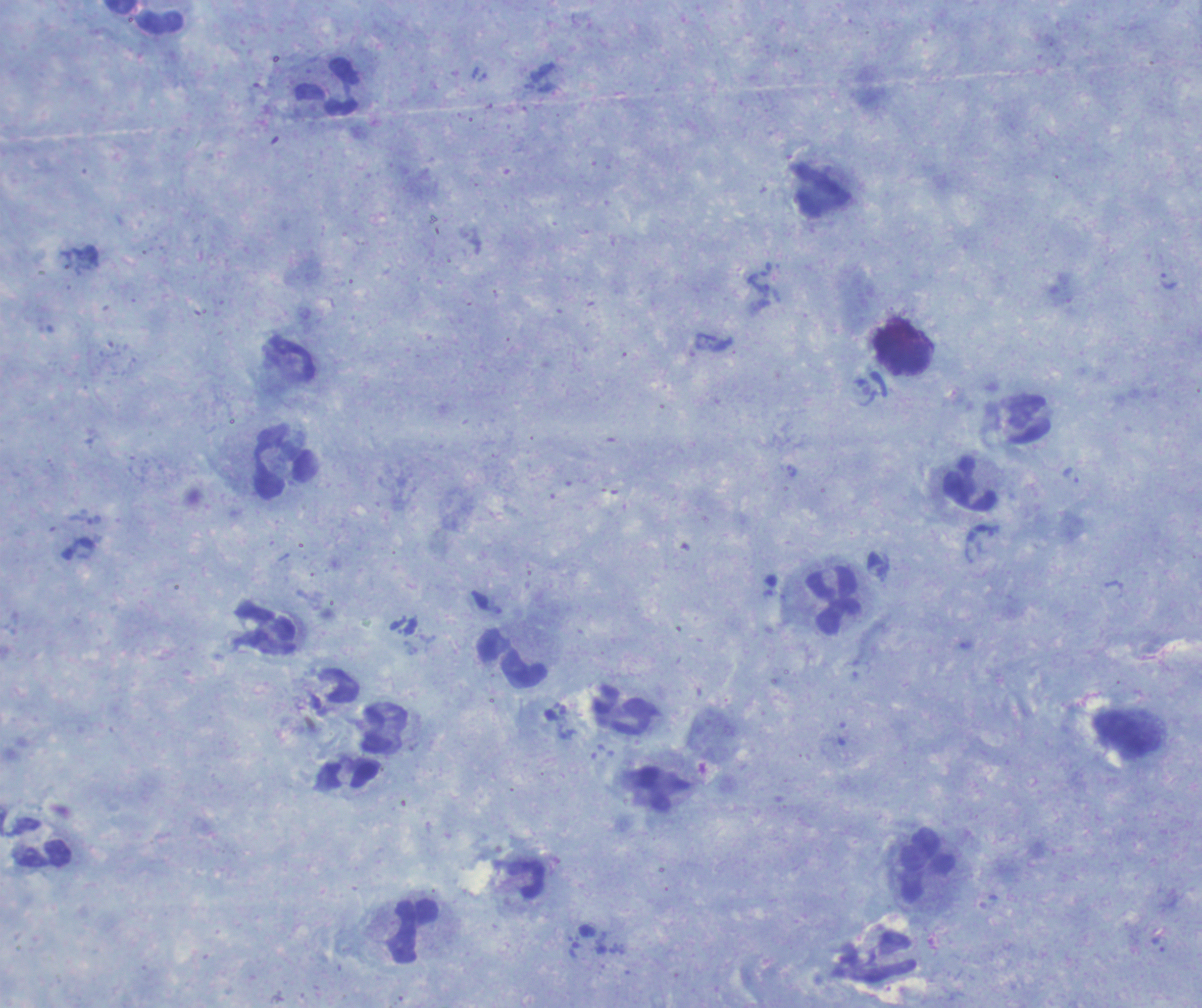
Approximate object centers, in pixels from the top-left corner. Trophozoite locations: (x=1168, y=281), (x=759, y=286), (x=791, y=471), (x=1071, y=475). Leukocyte locations: (x=143, y=16), (x=326, y=86), (x=821, y=189), (x=903, y=349), (x=286, y=461), (x=970, y=484), (x=833, y=601), (x=266, y=629), (x=512, y=659), (x=625, y=711), (x=348, y=776), (x=40, y=843), (x=926, y=865), (x=526, y=878), (x=415, y=931). Result: positive for malaria parasites. Background quality: satisfactory. Previously used in a real diagnosis. Single field of view. Romanowsky stain. Thick smear of blood. Image is 1202×1008 pixels. Captured at 100x magnification. Coloration quality: good.